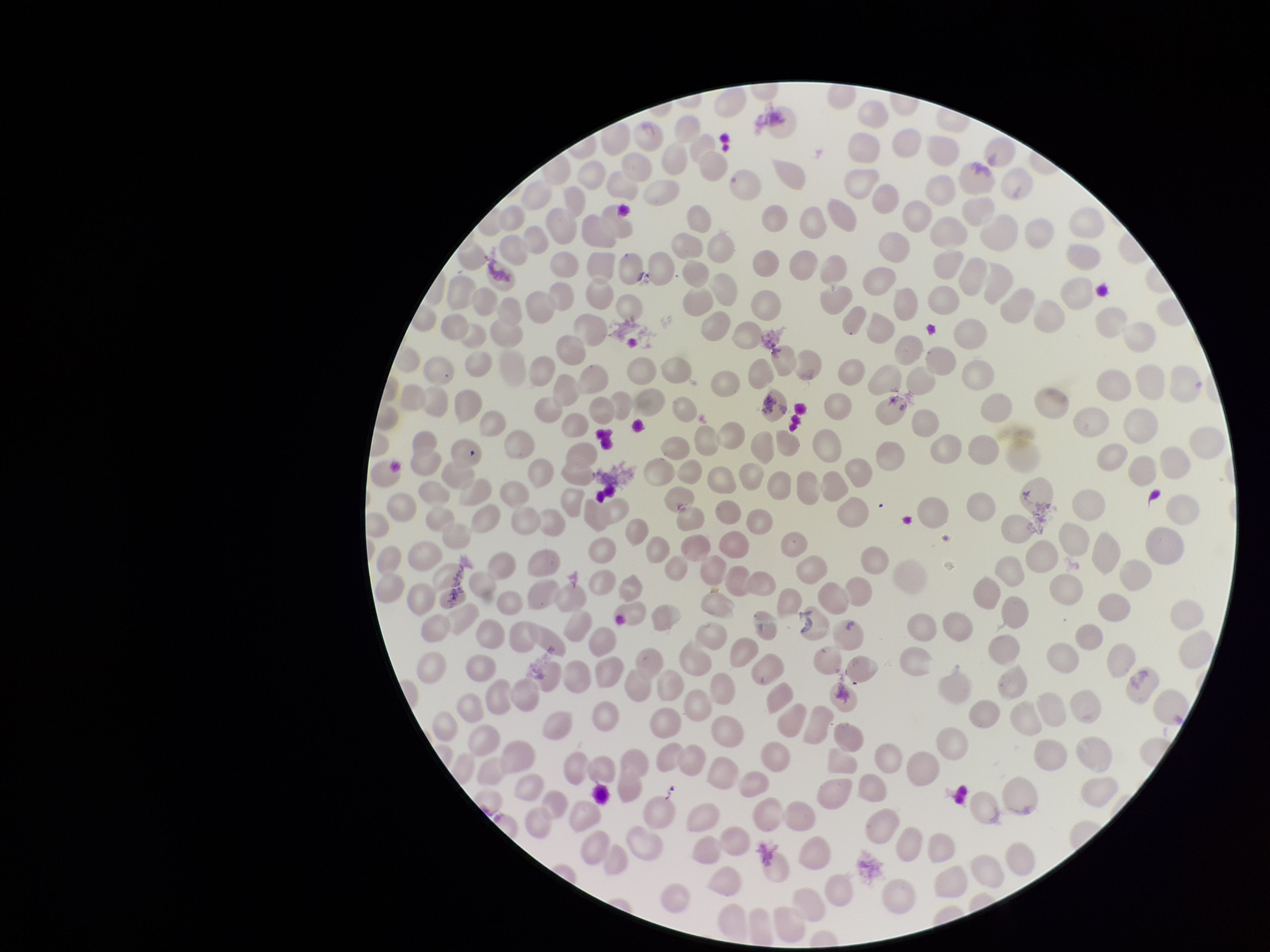 Giemsa stain. Parasitized red blood cells: none seen. Image is 1270×952 pixels. Patient malaria status: negative. Preparation: thin. One field from this slide. Red blood cell count: 249. Parasitized red blood cell count: 0. Smartphone photograph taken through the eyepiece of a microscope.